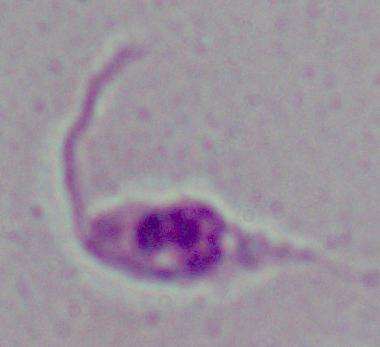

Summary:
  - Identification: Leishmania
  - Modality: micrograph
  - Magnification: 1000x